Identify the parasite.
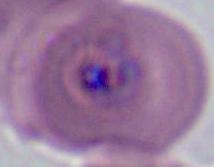
Plasmodium.

modality: micrograph
magnification: 400x or 1000x